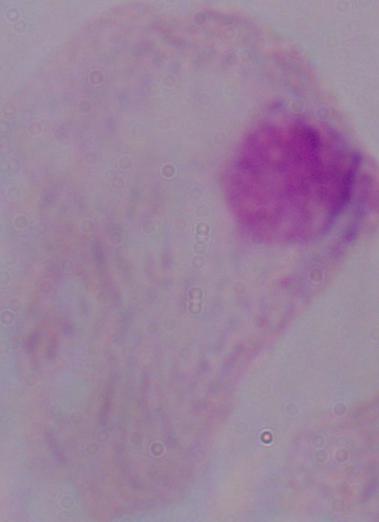
magnification: 1000x
identification: trichomonad
modality: micrograph